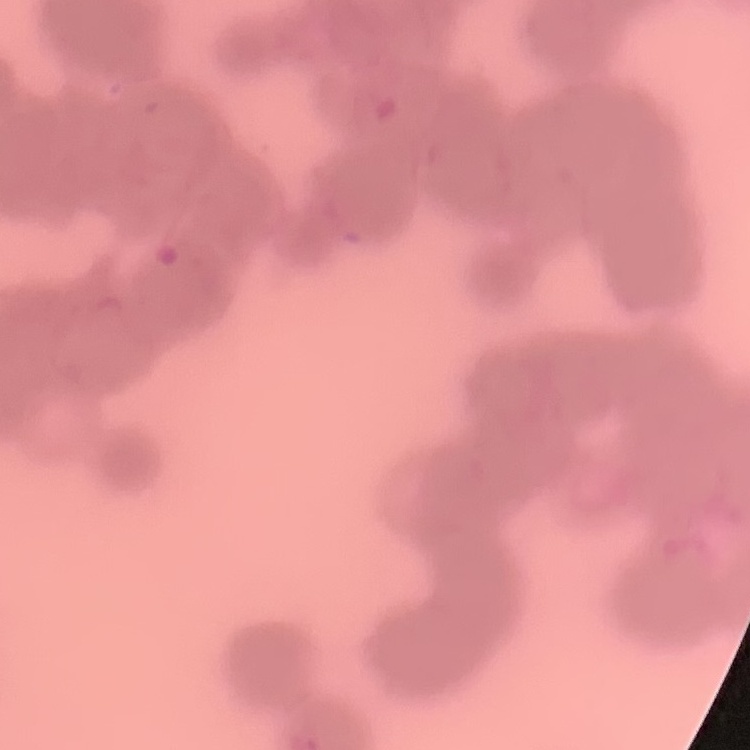

The erythrocytes exhibit rouleaux formation. Field's or Giemsa stain. Square crop of a larger photomicrograph. Thin blood film.